Classify this cell by malaria status.
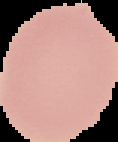
It is uninfected.

Image is 118×142 pixels. From a thin blood film. Cell region segmented out of the field of view; the surrounding area is masked to black.